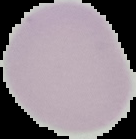

Summary:
  - Malaria status: uninfected
  - Image size: 136×139 pixels
  - Preparation: thin blood film
  - Image type: cell region segmented out of the field of view; surrounding area masked to black